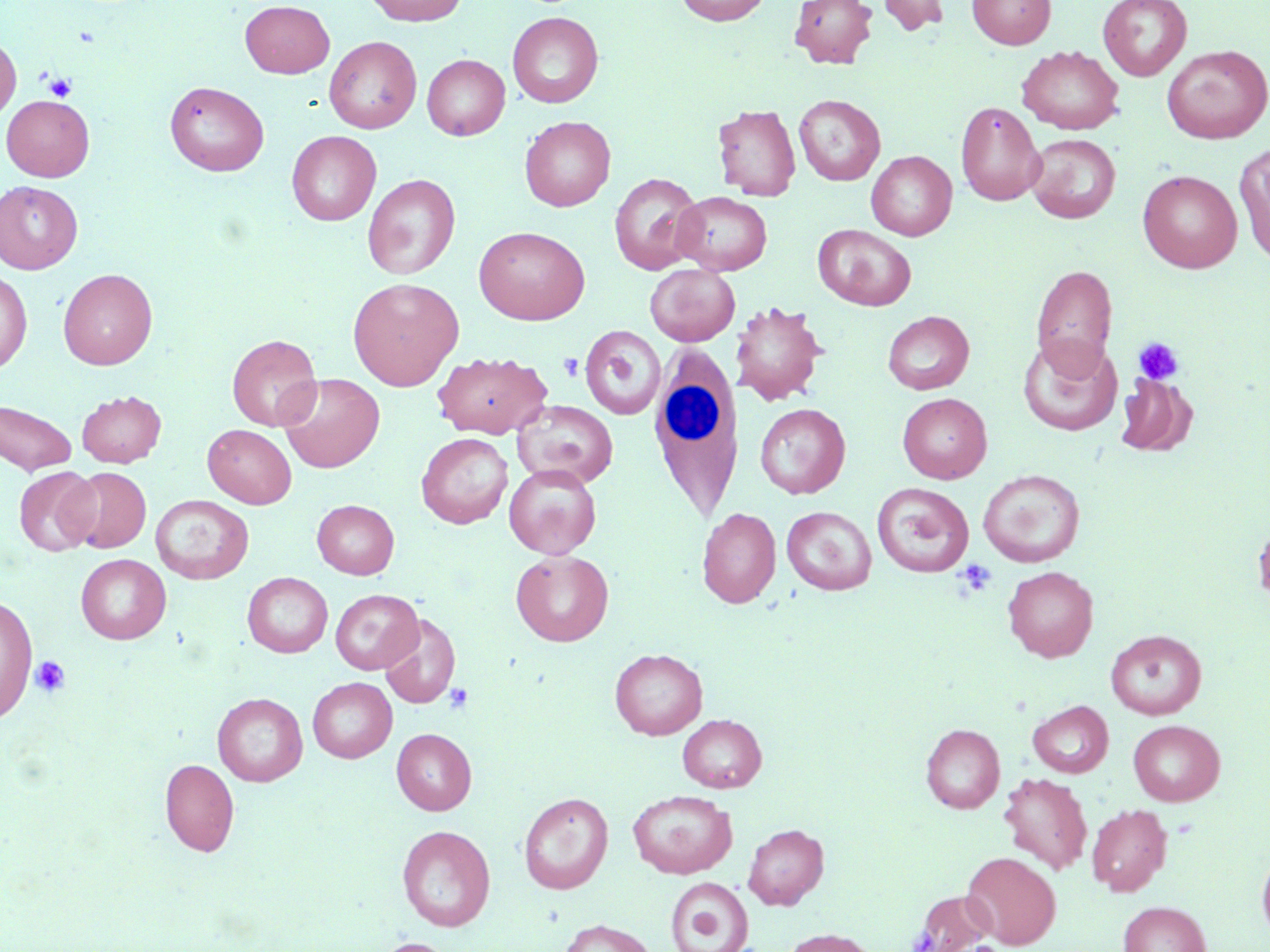

Summary:
  - Coordinate format: approximate bounding boxes as [x1, y1, x2, y2] in pixels
  - Uninfected red blood cell locations: [363, 0, 468, 26], [675, 0, 771, 25], [789, 0, 877, 69], [876, 0, 950, 36], [967, 0, 1055, 49], [1098, 0, 1192, 81], [240, 1, 335, 78], [507, 12, 604, 108], [0, 36, 21, 123], [324, 36, 421, 133], [1018, 45, 1124, 134], [1162, 45, 1270, 144], [422, 54, 510, 140], [164, 80, 269, 176], [794, 94, 885, 185], [1, 95, 95, 181], [956, 101, 1046, 206], [712, 104, 801, 201], [519, 116, 615, 211], [287, 130, 381, 225], [1025, 134, 1121, 223], [1234, 142, 1270, 266], [866, 151, 956, 240], [1137, 170, 1242, 273], [363, 173, 460, 280], [609, 173, 704, 274], [0, 180, 83, 273], [672, 191, 772, 274], [813, 224, 916, 311], [474, 226, 590, 325], [645, 263, 740, 346], [1031, 264, 1118, 374], [58, 268, 158, 370], [0, 270, 32, 374], [347, 277, 464, 390], [732, 300, 827, 406], [882, 310, 974, 395], [580, 324, 666, 420], [227, 334, 321, 431], [1019, 334, 1120, 437], [433, 351, 553, 439], [278, 373, 385, 473], [1116, 373, 1197, 456], [76, 390, 166, 467], [898, 393, 992, 483], [0, 400, 77, 475], [512, 400, 618, 488], [755, 403, 851, 499], [203, 424, 297, 508], [416, 433, 513, 528], [504, 464, 601, 559], [13, 466, 100, 556], [64, 467, 151, 553], [978, 469, 1085, 567], [872, 483, 974, 577], [151, 495, 254, 584], [312, 499, 399, 579], [781, 506, 876, 595], [697, 508, 781, 608], [1253, 514, 1270, 614], [511, 550, 613, 646], [76, 554, 171, 644], [1003, 566, 1098, 661], [242, 572, 333, 658], [330, 589, 423, 674], [0, 595, 38, 721], [380, 613, 461, 709], [1105, 630, 1207, 719], [610, 648, 707, 739], [308, 677, 397, 762], [212, 692, 307, 786], [1028, 700, 1113, 778], [678, 714, 767, 792], [1128, 720, 1225, 806], [921, 723, 1005, 813], [392, 729, 476, 815], [160, 758, 239, 856], [999, 772, 1092, 874], [628, 790, 737, 879], [518, 792, 614, 894], [1087, 803, 1173, 896], [743, 823, 829, 909], [397, 824, 495, 931], [1257, 847, 1270, 943], [962, 851, 1061, 949], [665, 877, 753, 952], [906, 889, 999, 952], [1118, 901, 1212, 952], [557, 919, 657, 952], [780, 928, 879, 952], [372, 937, 459, 952]
  - Platelet locations: [43, 73, 76, 102], [1133, 337, 1184, 385], [559, 353, 583, 381], [955, 560, 996, 598], [31, 656, 70, 696], [443, 683, 474, 714]
  - White blood cell locations: [646, 349, 745, 522]
  - Slide-level diagnosis: no evidence of blood parasites
  - Modality: light microscopy
  - Image size: 1270×952 pixels
  - Magnification: 1000x
  - Preparation: thin blood smear
  - Field of view: one of a larger specimen
  - Stain: May-Grünwald-Giemsa